Outline each Plasmodium ovale-infected red blood cell.
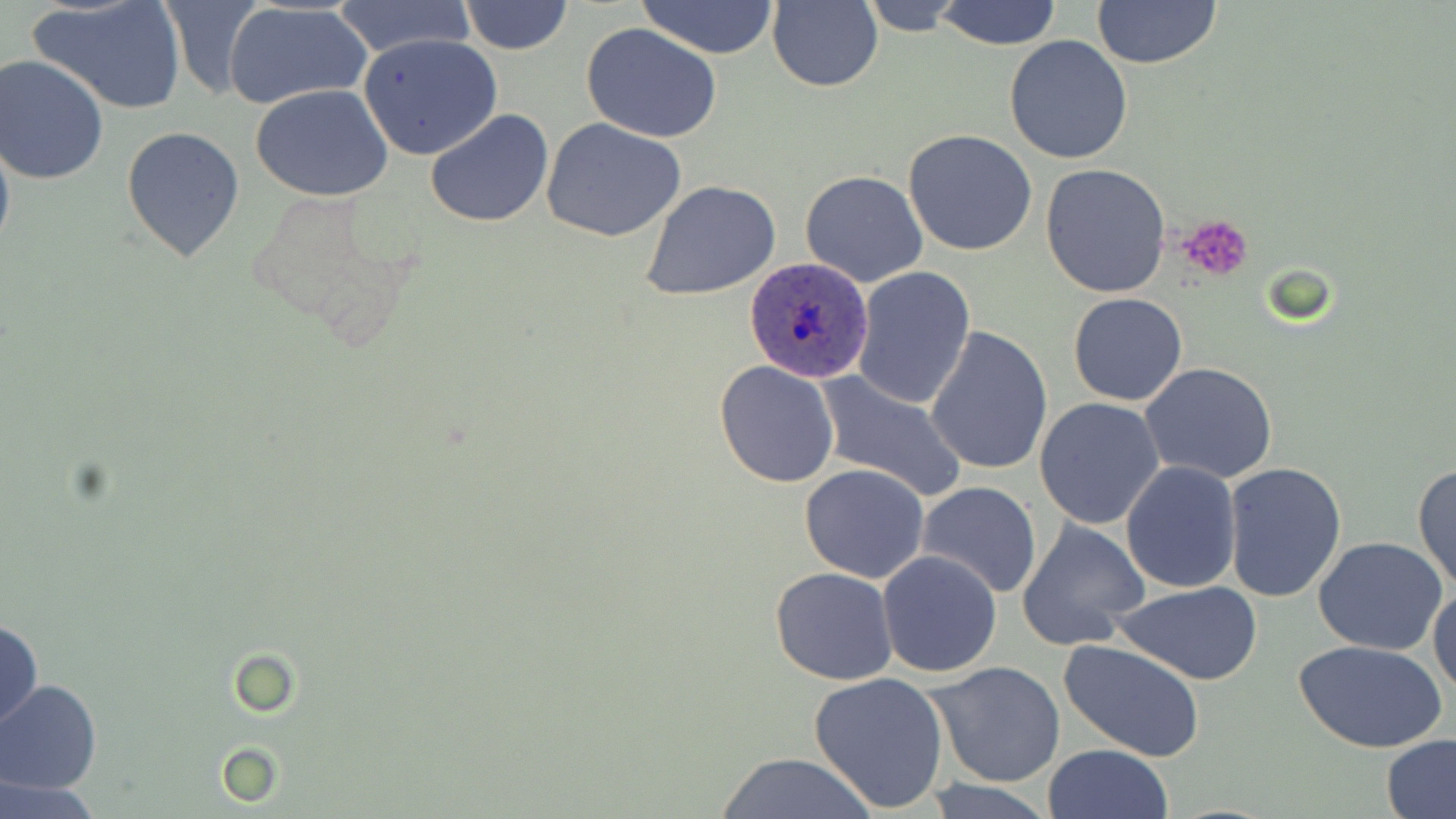
Approximate bounding boxes as named x1/y1/x2/y2 corners in pixels.
Plasmodium ovale-infected red blood cells: (x1=745, y1=256, x2=875, y2=384).

Summary:
  - Uninfected red blood cell locations: (x1=28, y1=0, x2=189, y2=117), (x1=636, y1=0, x2=781, y2=58), (x1=330, y1=1, x2=477, y2=59), (x1=457, y1=1, x2=573, y2=55), (x1=858, y1=1, x2=969, y2=33), (x1=932, y1=1, x2=1063, y2=49), (x1=1092, y1=1, x2=1221, y2=70), (x1=221, y1=2, x2=372, y2=111), (x1=767, y1=2, x2=883, y2=92), (x1=581, y1=21, x2=723, y2=143), (x1=358, y1=34, x2=501, y2=160), (x1=1004, y1=36, x2=1133, y2=164), (x1=0, y1=55, x2=109, y2=184), (x1=252, y1=85, x2=395, y2=201), (x1=425, y1=108, x2=553, y2=228), (x1=542, y1=119, x2=689, y2=243), (x1=121, y1=126, x2=247, y2=265), (x1=0, y1=127, x2=14, y2=264), (x1=903, y1=129, x2=1037, y2=256), (x1=1041, y1=164, x2=1172, y2=298), (x1=799, y1=170, x2=929, y2=288), (x1=640, y1=179, x2=781, y2=301), (x1=850, y1=266, x2=976, y2=408), (x1=1066, y1=293, x2=1188, y2=407), (x1=925, y1=325, x2=1054, y2=476), (x1=714, y1=360, x2=840, y2=486), (x1=1140, y1=362, x2=1279, y2=483), (x1=815, y1=371, x2=965, y2=503), (x1=1034, y1=397, x2=1166, y2=529), (x1=1119, y1=461, x2=1241, y2=594), (x1=1223, y1=462, x2=1347, y2=602), (x1=799, y1=463, x2=930, y2=584), (x1=1413, y1=464, x2=1456, y2=594), (x1=915, y1=482, x2=1042, y2=599), (x1=1016, y1=520, x2=1150, y2=650), (x1=1312, y1=537, x2=1449, y2=655), (x1=877, y1=551, x2=1004, y2=679), (x1=768, y1=566, x2=898, y2=685), (x1=1115, y1=582, x2=1262, y2=684), (x1=1428, y1=584, x2=1456, y2=697), (x1=1, y1=619, x2=43, y2=728), (x1=1057, y1=638, x2=1208, y2=764), (x1=1297, y1=639, x2=1449, y2=753), (x1=928, y1=661, x2=1066, y2=788), (x1=806, y1=671, x2=952, y2=814), (x1=0, y1=680, x2=101, y2=793), (x1=1381, y1=735, x2=1456, y2=819), (x1=1043, y1=744, x2=1172, y2=819), (x1=218, y1=745, x2=281, y2=805), (x1=710, y1=751, x2=876, y2=818), (x1=0, y1=777, x2=99, y2=819), (x1=915, y1=778, x2=1061, y2=819)
  - Platelet locations: (x1=1178, y1=216, x2=1255, y2=281)
  - Slide-level diagnosis: Plasmodium ovale
  - Image size: 1456×819 pixels
  - Field of view: one of a larger specimen
  - Modality: light microscopy
  - Preparation: thin blood film
  - Stain: May-Grünwald-Giemsa
  - Magnification: 1000x